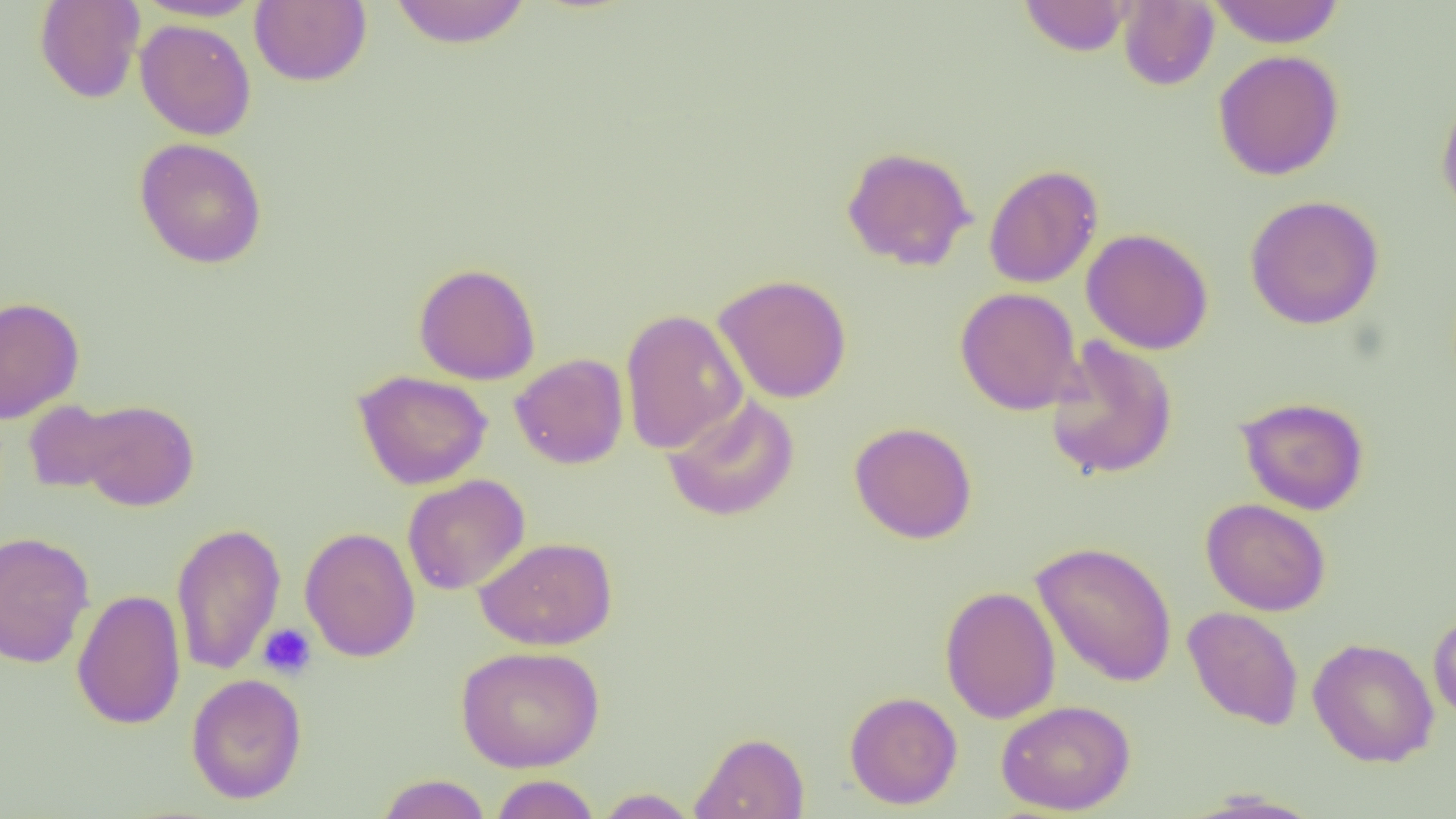

Summary:
  - Coordinate format: approximate bounding boxes as (x1, y1, x2, y2) in pixels
  - Platelet locations: (258, 623, 317, 679)
  - Uninfected red blood cell locations: (34, 0, 145, 104), (133, 0, 266, 22), (250, 0, 371, 87), (1019, 0, 1133, 56), (1207, 0, 1345, 47), (388, 1, 531, 48), (1118, 1, 1219, 91), (135, 19, 257, 141), (1213, 49, 1344, 180), (1436, 90, 1456, 222), (134, 137, 267, 269), (841, 145, 977, 271), (983, 163, 1103, 289), (1244, 194, 1384, 330), (1082, 227, 1214, 354), (413, 262, 541, 385), (712, 273, 852, 403), (955, 287, 1083, 415), (0, 295, 84, 424), (620, 308, 748, 454), (1045, 335, 1178, 481), (510, 353, 628, 469), (353, 369, 492, 490), (662, 394, 800, 522), (1235, 396, 1370, 515), (72, 399, 199, 512), (22, 400, 135, 494), (849, 421, 977, 544), (402, 474, 530, 595), (1201, 498, 1331, 616), (170, 521, 286, 675), (299, 526, 420, 662), (0, 531, 95, 669), (474, 536, 618, 650), (1031, 540, 1177, 687), (940, 585, 1061, 724), (71, 588, 186, 730), (1182, 606, 1304, 731), (1429, 608, 1456, 725), (1308, 637, 1439, 767), (455, 645, 605, 772), (186, 673, 307, 804), (844, 691, 963, 809), (996, 699, 1136, 815), (690, 731, 810, 818), (375, 774, 493, 818), (489, 774, 600, 818), (594, 787, 701, 818)
  - Slide-level diagnosis: negative for blood parasites
  - Modality: light microscopy
  - Preparation: thin blood smear
  - Field of view: single
  - Image size: 1456×819 pixels
  - Magnification: 1000x